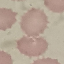

Malaria status: uninfected. Photographed with a smartphone camera at the microscope eyepiece. Thin smear of blood. Cell patch, automatically extracted from a larger field of view and resized to 64 × 64 pixels. Giemsa stain.